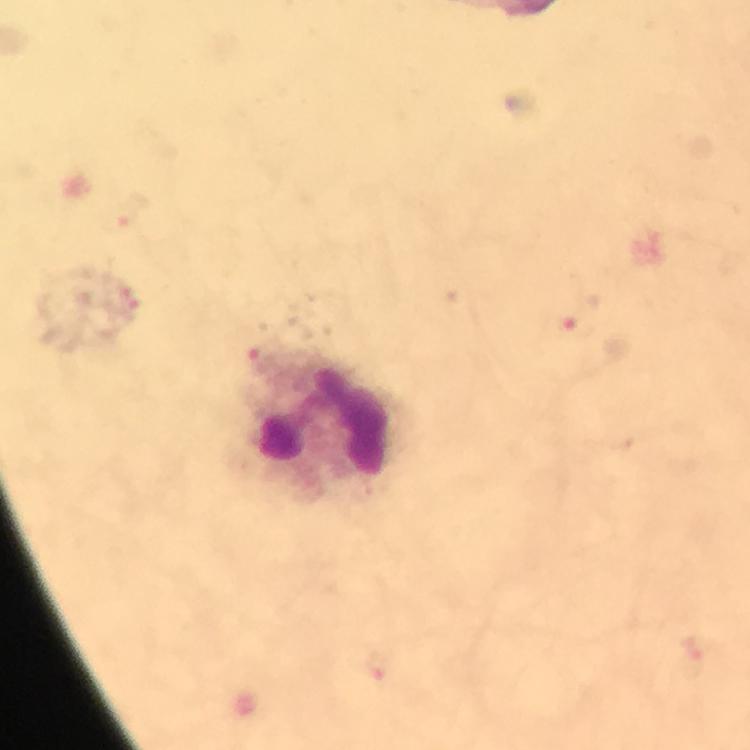
Approximate centers as [x, y] in pixels.
Summary:
  - Leukocyte locations: [324, 425]
  - Malaria parasite locations: [574, 327], [375, 662]
  - Image size: 750×750 pixels
  - Preparation: thick blood smear
  - Stain: Giemsa
  - Magnification: 100x
  - Capture: smartphone camera through the microscope
  - Context: from a diagnostic examination for malaria
  - Immersion oil: applied
  - Cropped from: a single field of view